Describe the morphology of the red blood cells.
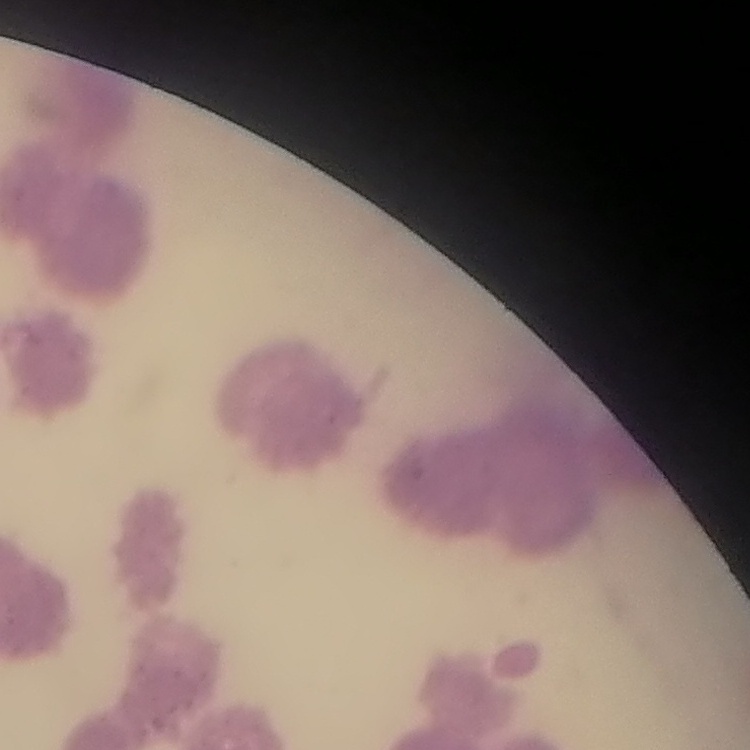
They show rouleaux formation.

preparation: thin peripheral smear
image_type: one tile cut from a larger photomicrograph
stain: Field's or Giemsa